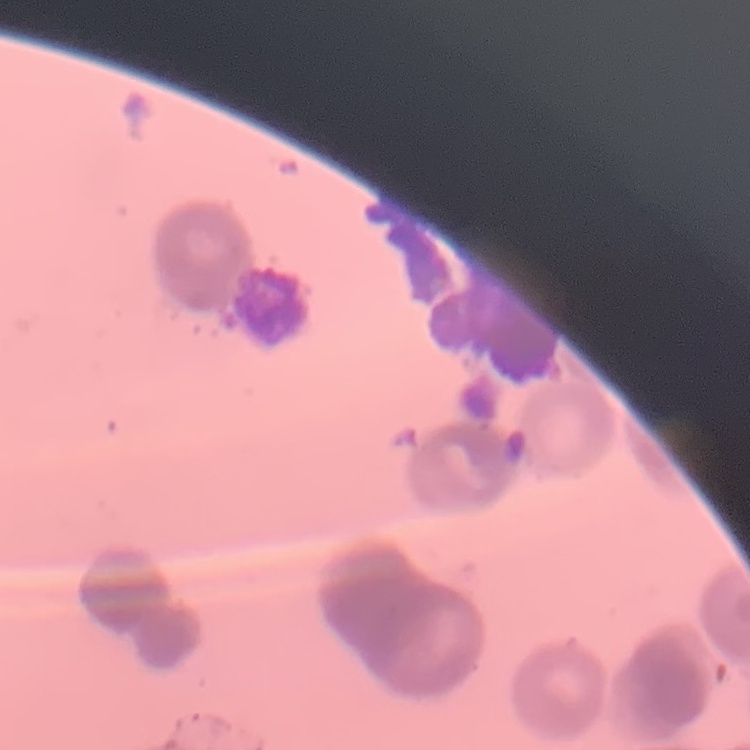
The erythrocytes exhibit rouleaux formation. One tile cut from a larger photomicrograph. Thin blood smear. Stained with either Field's or Giemsa.